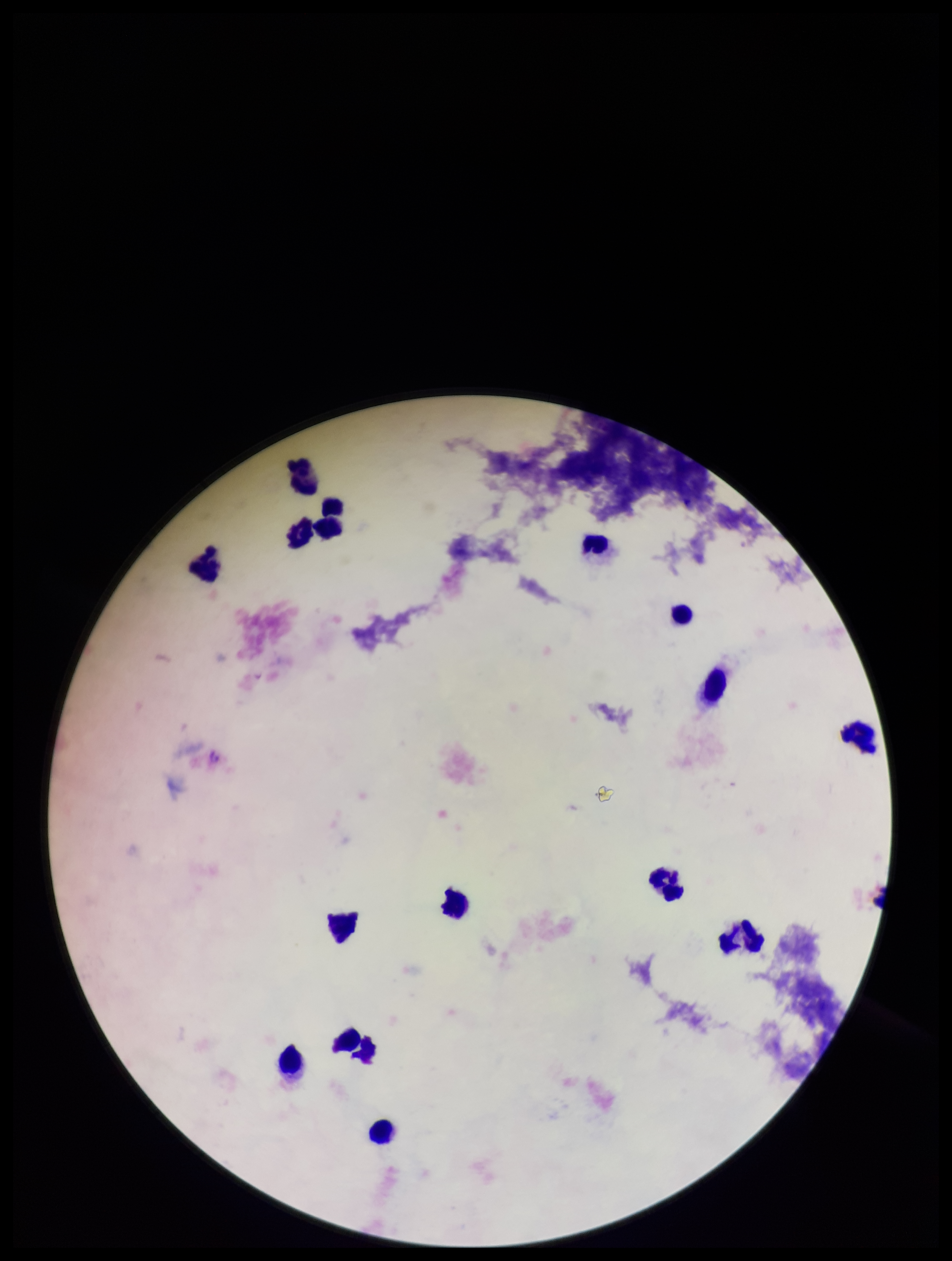

Giemsa stain. Plasmodium parasites: none seen. Image is 952×1261 pixels. Single field of view. Preparation: thick blood smear. Leukocyte count: 16. Patient malaria status: negative. Parasite count: 0. Smartphone photograph taken through the eyepiece of a microscope.